Outline each Plasmodium vivax-infected red blood cell.
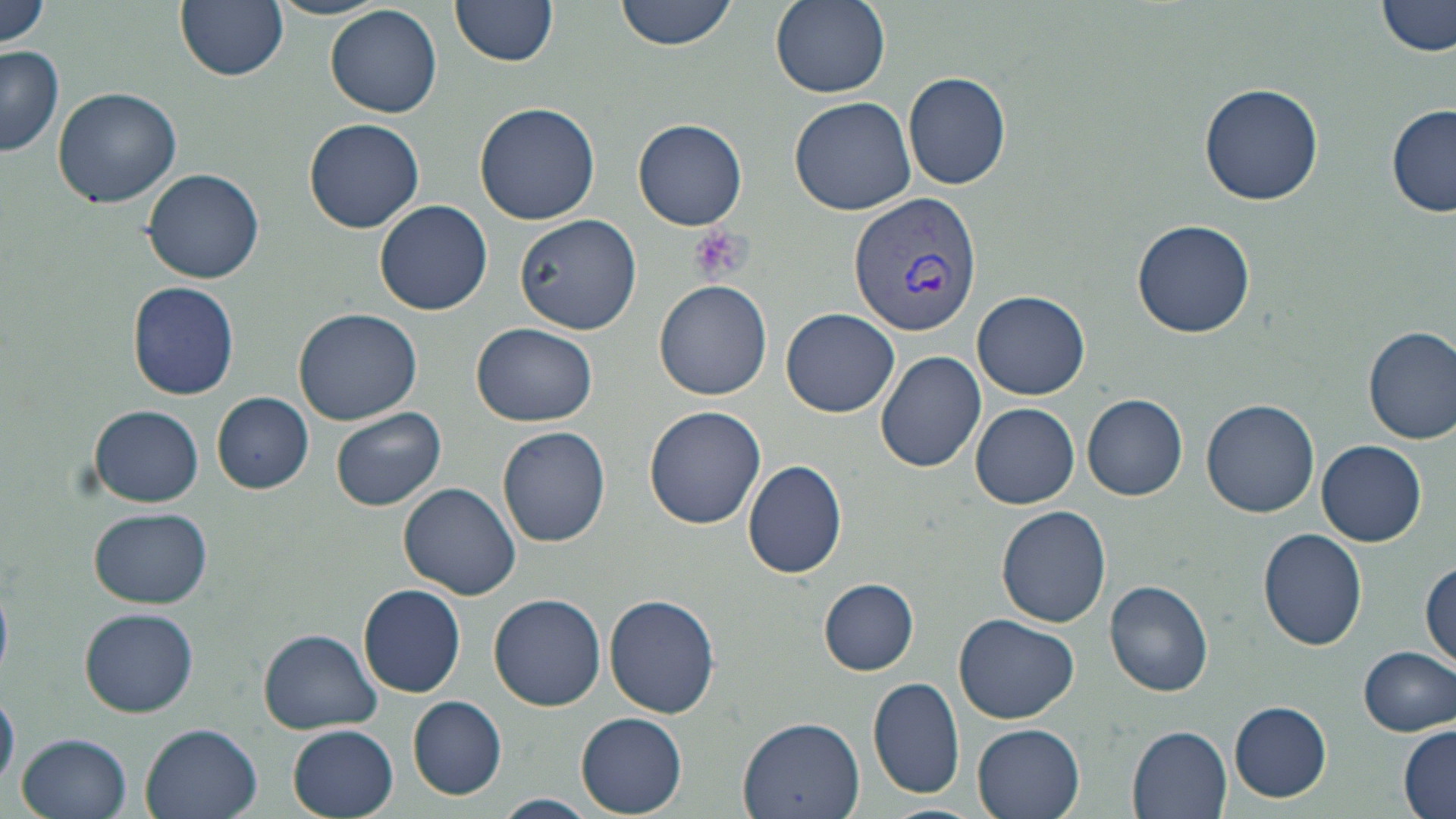
Approximate bounding boxes as (x1,y1)-(x2,y2) corner pairs in pixels.
Plasmodium vivax-infected red blood cells: (847,192)-(983,337).

{
  "slide_level_diagnosis": "Plasmodium vivax",
  "modality": "light microscopy",
  "field_of_view": "single",
  "stain": "May-Grünwald-Giemsa",
  "platelet_locations": "approximate bounding boxes as (x1,y1)-(x2,y2) corner pairs in pixels: (689,225)-(752,285)",
  "preparation": "thin blood smear",
  "magnification": "1000x",
  "image_size": "1456×819 pixels",
  "uninfected_red_blood_cell_locations": "approximate bounding boxes as (x1,y1)-(x2,y2) corner pairs in pixels: (0,0)-(53,50), (175,0)-(288,82), (267,0)-(394,21), (449,0)-(559,68), (615,0)-(734,51), (770,0)-(890,97), (1378,0)-(1456,59), (326,5)-(442,118), (0,46)-(65,157), (902,71)-(1011,190), (1199,82)-(1324,206), (53,86)-(181,208), (789,96)-(915,214), (474,103)-(600,223), (1386,104)-(1456,218), (304,118)-(425,234), (634,118)-(749,230), (142,169)-(265,284), (373,200)-(493,316), (515,212)-(641,336), (1132,217)-(1255,338), (655,278)-(772,400), (126,282)-(239,400), (973,291)-(1090,399), (292,307)-(422,426), (780,308)-(900,418), (470,324)-(601,426), (1363,326)-(1455,445), (877,350)-(987,473), (211,392)-(313,493), (1082,394)-(1187,501), (1202,399)-(1320,518), (971,403)-(1080,509), (88,404)-(204,507), (331,406)-(445,510), (642,406)-(766,531), (497,426)-(611,548), (1318,440)-(1426,545), (742,458)-(848,579), (399,483)-(522,601), (996,505)-(1112,628), (88,507)-(213,608), (1257,528)-(1368,651), (1421,554)-(1456,670), (820,579)-(918,675), (1104,579)-(1213,697), (357,583)-(465,696), (488,593)-(606,711), (604,593)-(719,718), (79,607)-(199,717), (953,612)-(1080,725), (258,628)-(384,733), (1361,645)-(1455,736), (867,676)-(965,802), (0,690)-(19,791), (408,697)-(506,800), (1230,701)-(1331,800), (575,711)-(688,815), (737,716)-(865,819), (971,721)-(1086,819), (1397,722)-(1455,819), (140,723)-(263,819), (288,725)-(400,817), (1126,725)-(1233,818), (17,733)-(132,819), (491,793)-(597,818), (880,803)-(988,819)"
}